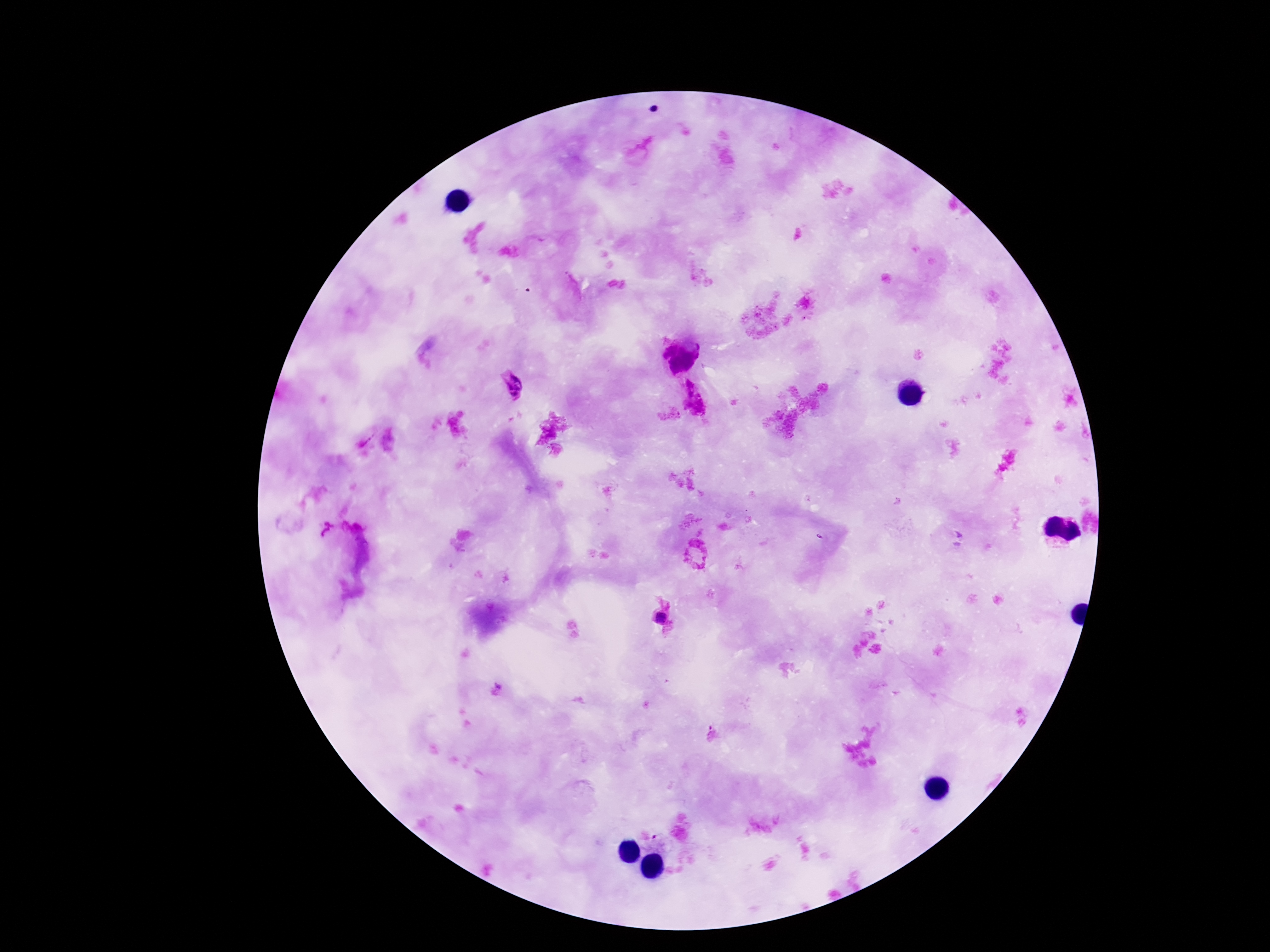

image size = 1270×952 pixels
capture = smartphone camera through the microscope eyepiece
field of view = single
stain = Giemsa
patient malaria status = infected
preparation = thick peripheral-blood smear
Plasmodium parasite locations = approximate object centers, in pixels from the top-left corner: (x=684, y=355), (x=513, y=381), (x=660, y=619), (x=496, y=691)
magnification = 100x